State which parasite is depicted.
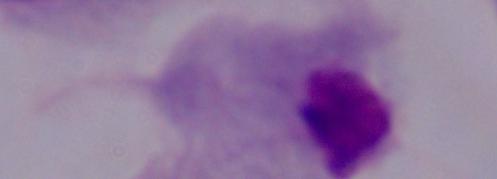
This is a trichomonad.

Photomicrograph. Captured at 1000x magnification.